Identify the parasite.
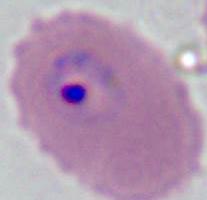

Plasmodium.

Photomicrograph. 400x or 1000x magnification.